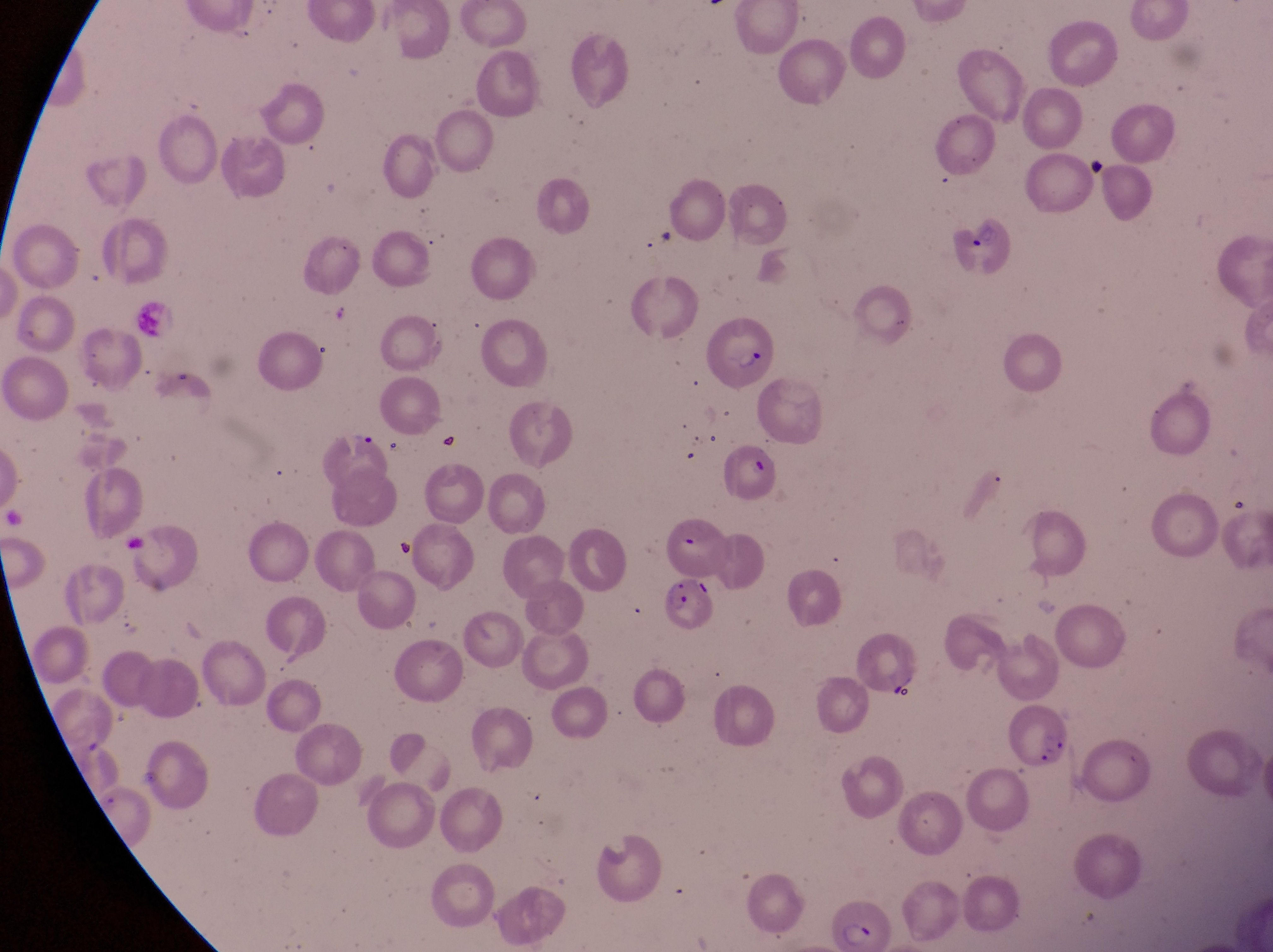
Approximate bounding boxes as left top right bottom in pixels. Artifact (platelet-like body, stain precipitate, or debris) locations: 1086 156 1109 179; 1225 492 1253 515; 886 681 929 709. Trophozoite locations: 349 422 376 452. Leukocyte locations: 134 296 180 346. Parasitised red blood cell locations: 949 204 1018 284; 704 313 778 391; 664 577 716 630; 1007 700 1078 773; 821 882 890 944. Magnification of 1000x. Thin blood film. Single field of view. Image is 1273×952 pixels. Sample from Uganda. Captured by a smartphone held over the eyepiece of an Olympus CX-23 microscope.